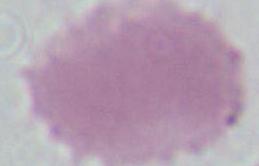
Captured at 1000x magnification. A red blood cell is shown. Photomicrograph.